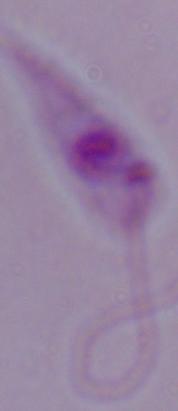 Photomicrograph. Captured at 1000x magnification. A Leishmania parasite is seen.